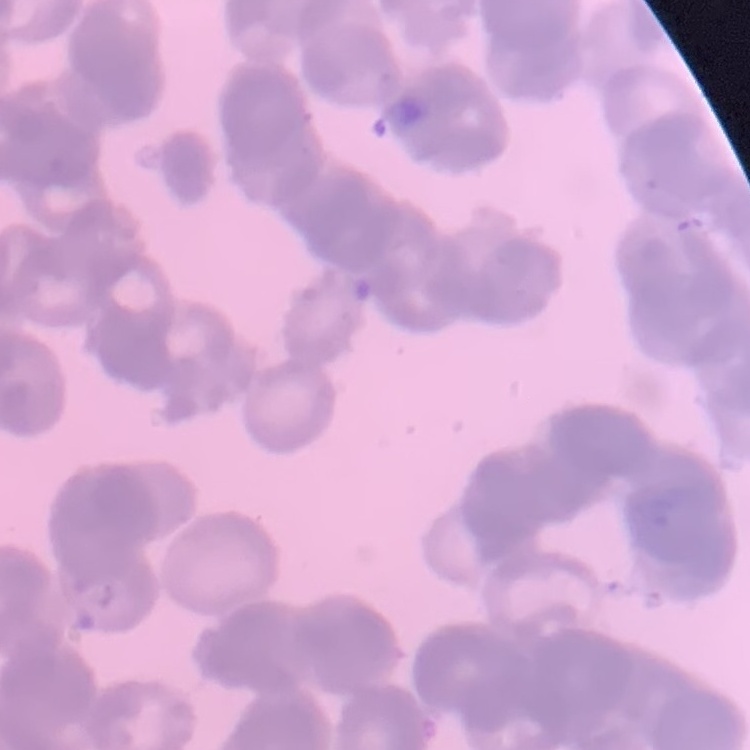

Summary:
  - Erythrocyte morphology: rouleaux formation
  - Preparation: thin peripheral smear
  - Image type: square crop of a larger photomicrograph
  - Stain: Field's or Giemsa